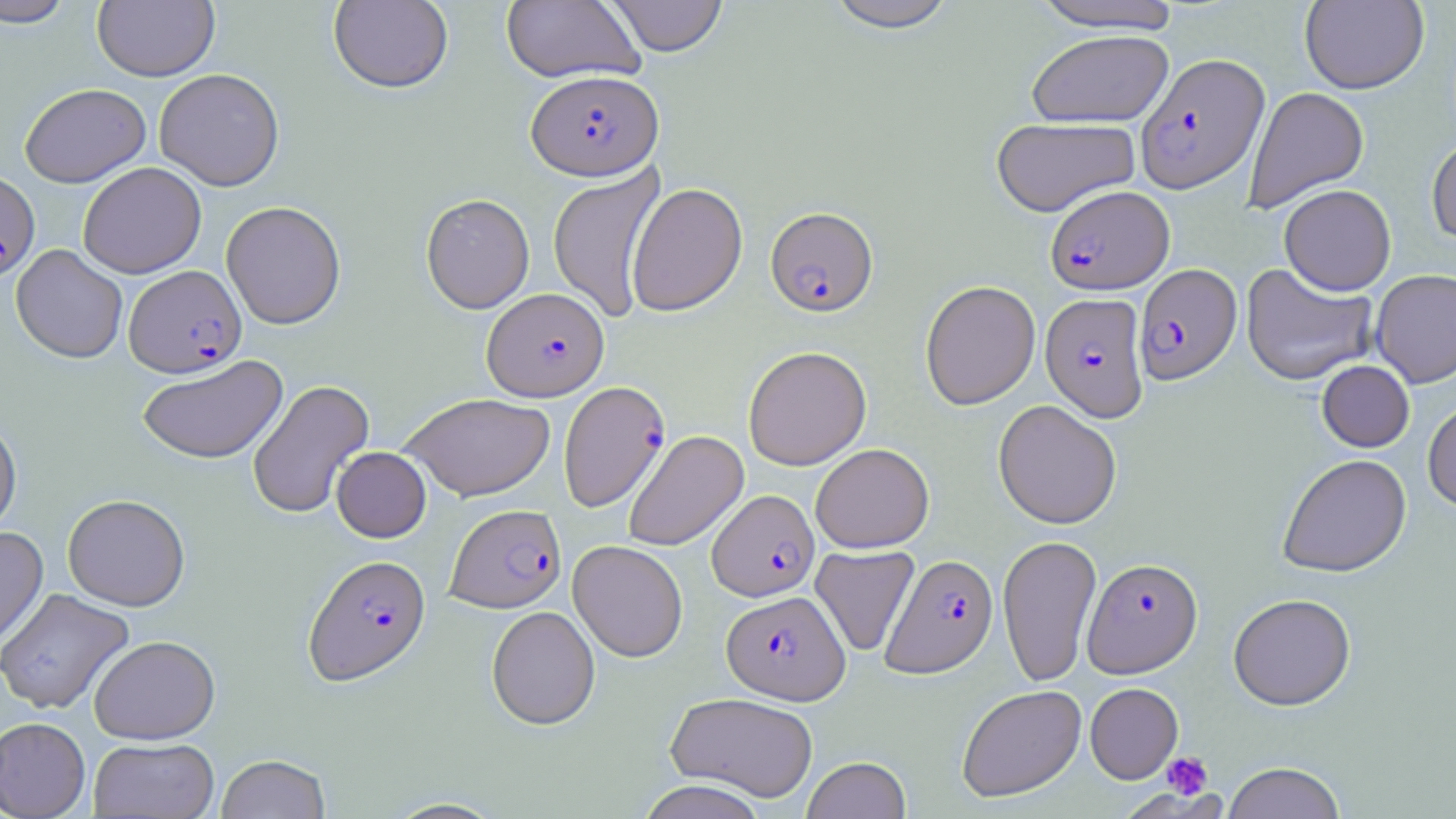

Summary:
  - Coordinate format: approximate bounding boxes as (x1, y1, x2, y2) in pixels
  - Plasmodium falciparum-infected red blood cell locations: (1135, 53, 1270, 193), (526, 69, 663, 180), (0, 169, 40, 280), (1045, 185, 1174, 294), (765, 205, 878, 316), (1133, 264, 1242, 385), (124, 265, 246, 378), (482, 287, 609, 401), (1040, 292, 1149, 422), (558, 381, 671, 512), (707, 489, 819, 601), (446, 504, 566, 613), (881, 553, 998, 678), (303, 554, 431, 686), (1083, 557, 1202, 677), (721, 590, 850, 704)
  - Platelet locations: (1162, 752, 1212, 799)
  - Uninfected red blood cell locations: (0, 0, 78, 28), (605, 0, 729, 57), (823, 0, 959, 32), (1028, 0, 1186, 33), (1299, 0, 1429, 94), (92, 1, 219, 82), (328, 1, 453, 94), (500, 1, 645, 83), (1027, 29, 1174, 128), (154, 68, 284, 191), (20, 83, 151, 187), (1243, 86, 1369, 213), (991, 116, 1141, 217), (1427, 135, 1456, 246), (78, 162, 206, 278), (547, 164, 667, 323), (627, 182, 747, 317), (1279, 184, 1396, 296), (421, 193, 535, 314), (221, 201, 346, 329), (11, 245, 127, 364), (1240, 262, 1378, 386), (1370, 268, 1456, 388), (920, 280, 1040, 410), (743, 346, 871, 470), (136, 355, 288, 464), (1317, 360, 1414, 452), (248, 379, 374, 520), (400, 393, 555, 501), (1423, 397, 1456, 512), (994, 400, 1122, 529), (0, 415, 21, 539), (623, 430, 749, 552), (810, 443, 934, 552), (331, 446, 431, 542), (1277, 453, 1412, 577), (62, 493, 190, 611), (0, 527, 48, 651), (998, 533, 1102, 687), (568, 540, 688, 662), (810, 545, 920, 656), (0, 588, 134, 715), (1228, 593, 1356, 710), (486, 606, 600, 730), (88, 634, 220, 744), (1085, 682, 1183, 783), (956, 684, 1086, 803), (665, 691, 819, 802), (0, 717, 90, 819), (88, 737, 219, 818), (216, 754, 331, 819), (802, 756, 911, 819), (1223, 762, 1345, 819), (637, 780, 770, 819), (383, 797, 508, 818)
  - Slide-level diagnosis: Plasmodium falciparum
  - Preparation: thin blood smear
  - Image size: 1456×819 pixels
  - Stain: May-Grünwald-Giemsa
  - Field of view: single
  - Magnification: 1000x
  - Modality: optical microscopy